Assess this cell for malaria.
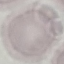

It is uninfected.

Summary:
  - Stain: Giemsa
  - Preparation: thin blood smear
  - Image type: automatically extracted cell patch, resized to 64 × 64 pixels
  - Capture: smartphone through the microscope eyepiece